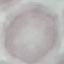
Summary:
  - Result: no malaria parasites seen
  - Capture: smartphone camera at the microscope eyepiece
  - Preparation: thin blood film
  - Stain: Giemsa
  - Image type: cell patch, automatically extracted from a larger field of view and resized to 64 × 64 pixels